Evaluate for Plasmodium parasites.
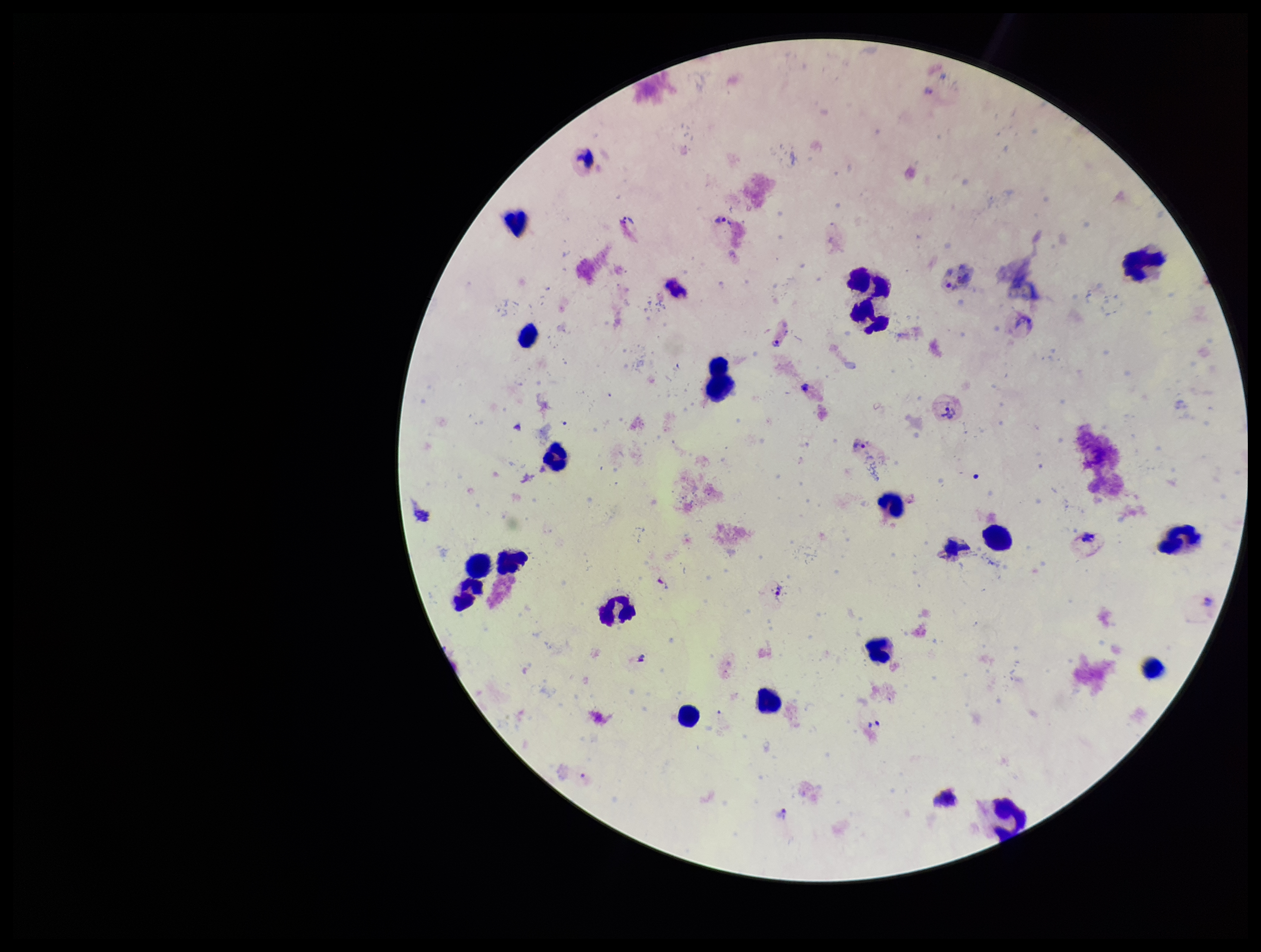
Identified.

Summary:
  - Parasite count: 12
  - Stain: Giemsa
  - Species reported for this patient: Plasmodium vivax
  - Capture: smartphone photograph through the microscope eyepiece
  - Field of view: one from this slide
  - Patient malaria status: positive
  - Leukocyte count: 20
  - Image size: 1261×952 pixels
  - Preparation: thick